Report the malaria status of this cell.
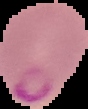
Parasitized.

Image is 88×109 pixels. From a thin blood smear. Cell region segmented out of the field of view; the surrounding area is masked to black.